Classify this cell by malaria status.
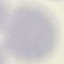

It is uninfected.

Summary:
  - Capture: smartphone through the microscope eyepiece
  - Preparation: thin smear
  - Stain: Giemsa
  - Image type: cell patch, automatically extracted from a larger field of view and resized to 64 × 64 pixels